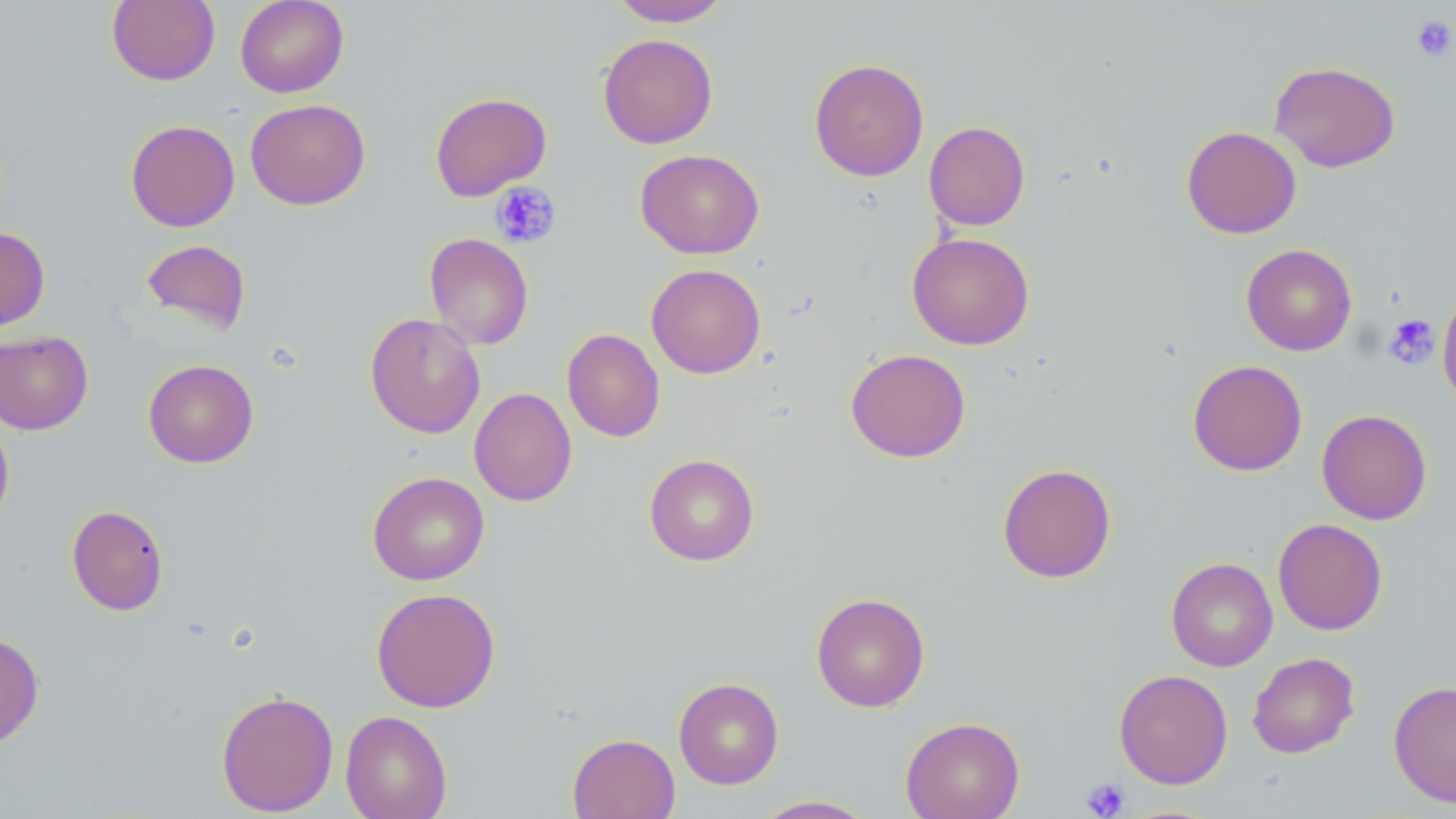
slide-level diagnosis = no evidence of blood parasites
preparation = thin blood smear
platelet locations (subset) = approximate bounding boxes as named x1/y1/x2/y2 corners in pixels: (x1=1411, y1=15, x2=1455, y2=62), (x1=491, y1=181, x2=561, y2=248), (x1=1382, y1=314, x2=1440, y2=370), (x1=1082, y1=778, x2=1131, y2=818)
uninfected red blood cell locations (subset) = approximate bounding boxes as named x1/y1/x2/y2 corners in pixels: (x1=107, y1=0, x2=220, y2=86), (x1=235, y1=0, x2=349, y2=97), (x1=610, y1=0, x2=732, y2=27), (x1=597, y1=33, x2=718, y2=149), (x1=808, y1=58, x2=929, y2=181), (x1=1270, y1=61, x2=1401, y2=173), (x1=245, y1=98, x2=371, y2=210), (x1=125, y1=119, x2=240, y2=232), (x1=924, y1=121, x2=1031, y2=231), (x1=1181, y1=125, x2=1302, y2=239), (x1=635, y1=149, x2=764, y2=259), (x1=0, y1=227, x2=50, y2=331), (x1=907, y1=232, x2=1035, y2=350), (x1=424, y1=233, x2=534, y2=350), (x1=141, y1=239, x2=252, y2=335), (x1=1241, y1=243, x2=1357, y2=356), (x1=646, y1=264, x2=766, y2=379), (x1=1437, y1=288, x2=1456, y2=409), (x1=365, y1=312, x2=486, y2=438), (x1=562, y1=328, x2=665, y2=442), (x1=0, y1=330, x2=93, y2=435), (x1=845, y1=348, x2=971, y2=462), (x1=143, y1=359, x2=259, y2=468), (x1=1187, y1=359, x2=1308, y2=477), (x1=469, y1=387, x2=577, y2=506), (x1=1317, y1=409, x2=1432, y2=524), (x1=0, y1=416, x2=14, y2=532), (x1=644, y1=454, x2=759, y2=566), (x1=997, y1=463, x2=1116, y2=583), (x1=368, y1=471, x2=490, y2=585), (x1=67, y1=504, x2=168, y2=616), (x1=1272, y1=518, x2=1387, y2=635), (x1=1166, y1=557, x2=1278, y2=671), (x1=371, y1=587, x2=501, y2=712), (x1=811, y1=592, x2=930, y2=712), (x1=0, y1=630, x2=44, y2=751), (x1=1247, y1=652, x2=1360, y2=759), (x1=1114, y1=668, x2=1233, y2=789), (x1=673, y1=677, x2=784, y2=789), (x1=1388, y1=680, x2=1456, y2=807), (x1=216, y1=689, x2=339, y2=816), (x1=340, y1=710, x2=452, y2=819), (x1=900, y1=716, x2=1024, y2=819), (x1=567, y1=733, x2=680, y2=819), (x1=753, y1=795, x2=878, y2=818)
modality = light microscopy
magnification = 1000x
stain = May-Grünwald-Giemsa
field of view = one of a larger specimen
image size = 1456×819 pixels